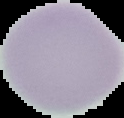

{
  "image_type": "segmented cell region with the area outside set to black",
  "preparation": "thin blood film",
  "image_size": "124×118 pixels",
  "result": "negative for Plasmodium parasites"
}